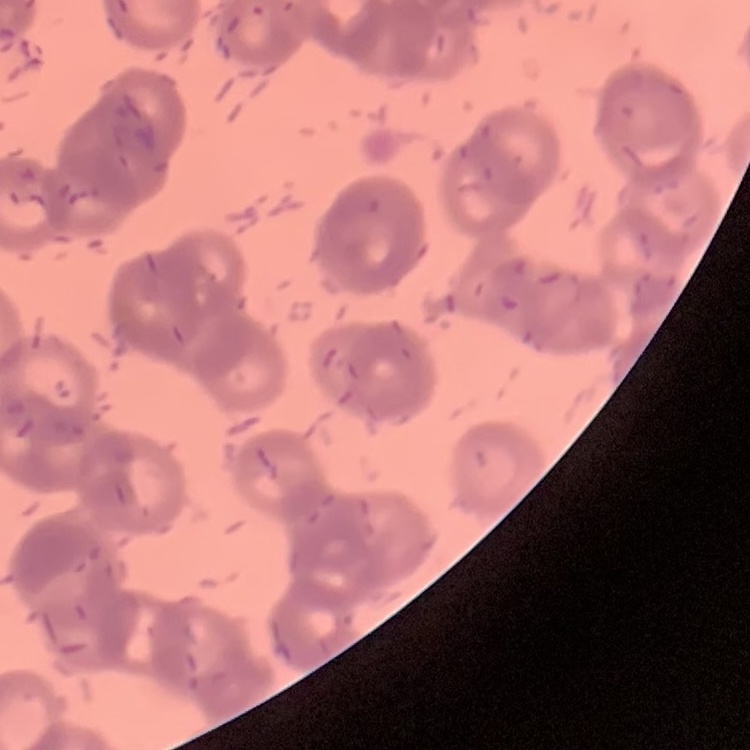 The red blood cells show rouleaux formation. One tile cut from a larger photomicrograph. Field's or Giemsa stain. Thin blood film.